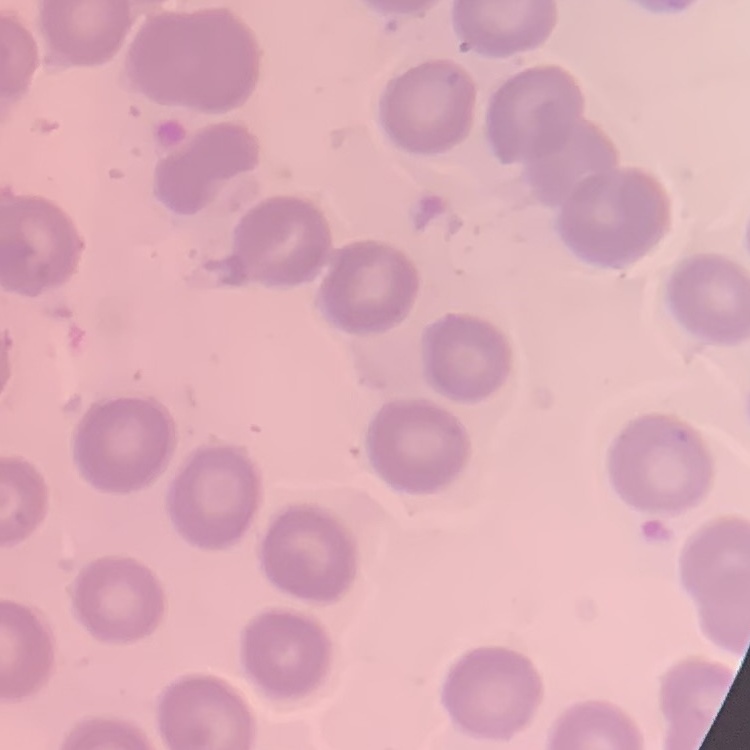
erythrocyte morphology = no rouleaux formation
preparation = thin blood smear
image type = square crop of a larger photomicrograph
stain = Field's or Giemsa